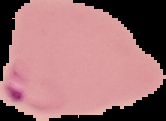

Summary:
  - Image type: cell region segmented out of the field of view; surrounding area masked to black
  - Malaria status: parasitized
  - Preparation: thin blood film
  - Image size: 166×121 pixels